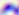

Summary:
  - Identification: Toxoplasma gondii
  - Modality: photomicrograph
  - Magnification: 400x